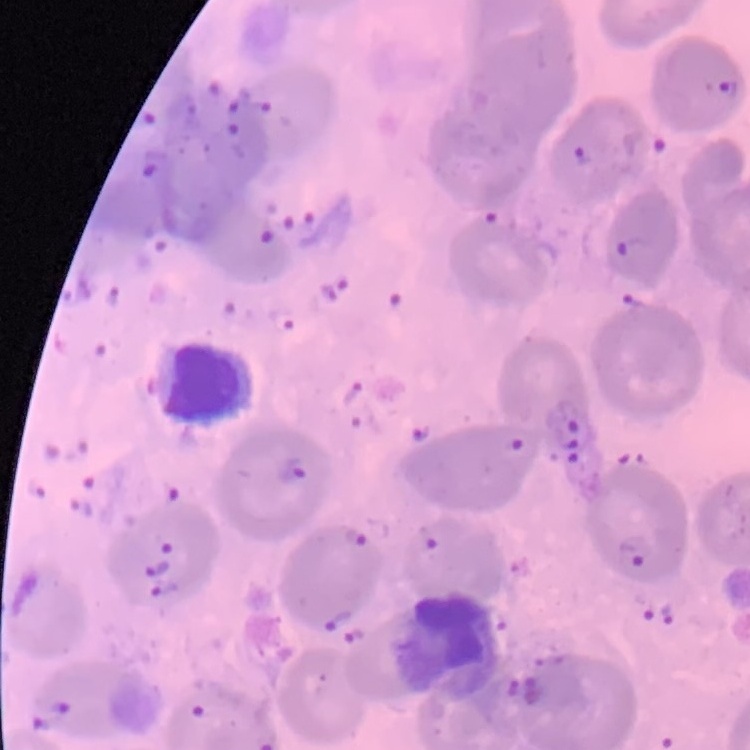

Summary:
  - Red blood cell morphology: no rouleaux formation
  - Stain: Field's or Giemsa
  - Preparation: thin blood film
  - Image type: square crop of a larger photomicrograph